Name the parasite shown.
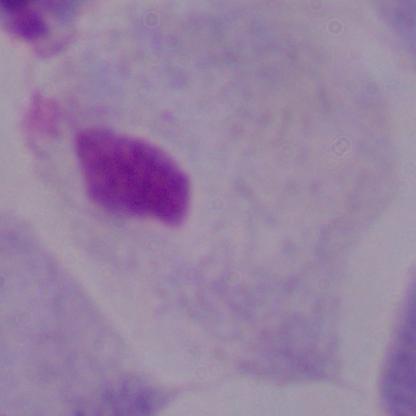
This is a trichomonad.

Micrograph. 1000x magnification.